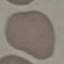

malaria status = uninfected
capture = smartphone through the microscope eyepiece
image type = cell patch, automatically extracted from a larger field of view and resized to 64 × 64 pixels
preparation = thin blood film
stain = Giemsa